Outline each blood parasite and name the species.
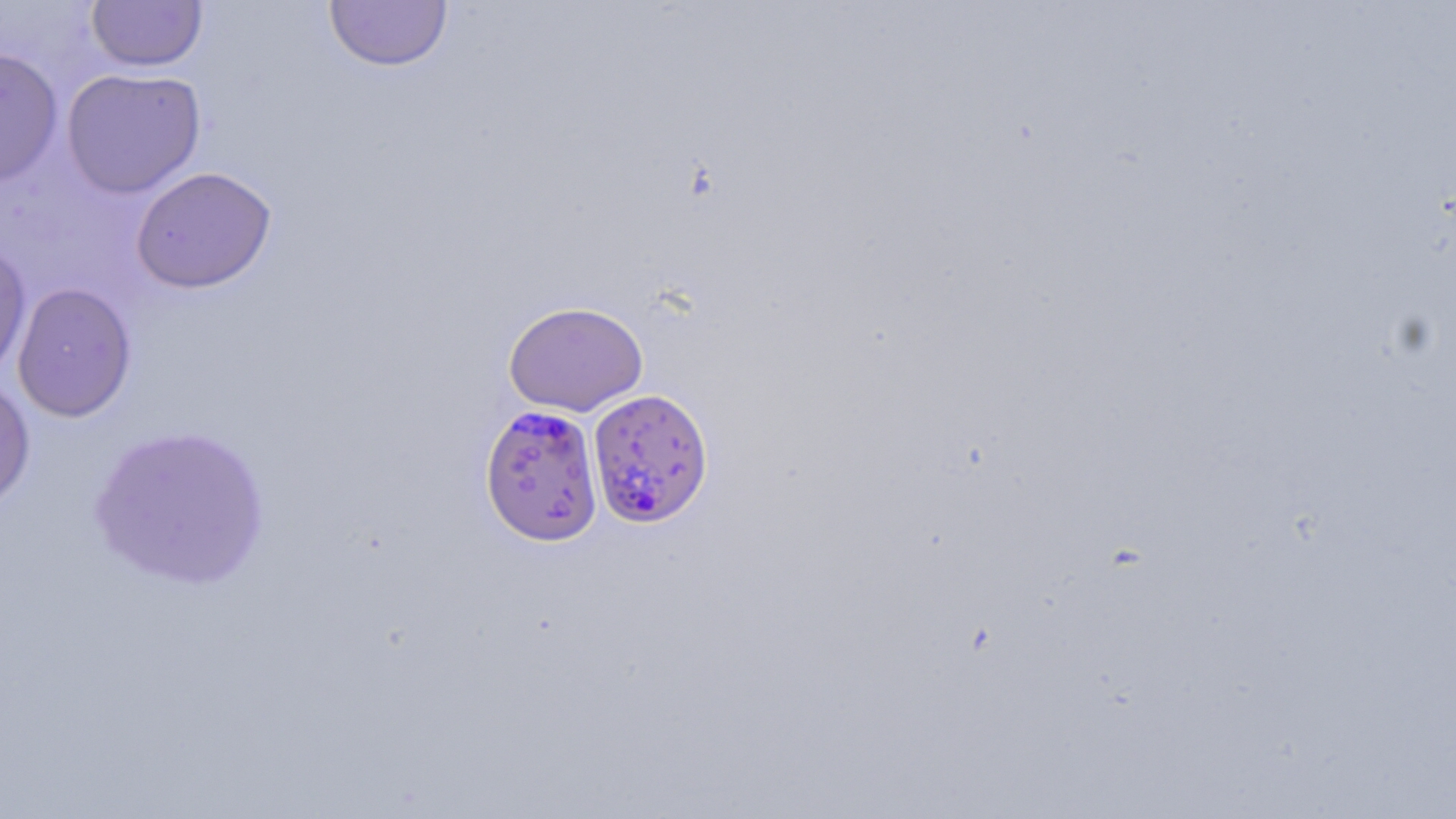

Approximate bounding boxes as (x1, y1, x2, y2) in pixels.
Plasmodium falciparum-infected red blood cells: (587, 388, 714, 528), (479, 404, 604, 546).
No Plasmodium ovale, Plasmodium malariae, Plasmodium vivax, Babesia divergens, or Trypanosoma brucei observed.

Uninfected red blood cell locations: (86, 0, 208, 72), (324, 1, 453, 72), (0, 46, 64, 188), (61, 67, 207, 199), (130, 166, 277, 294), (0, 240, 32, 382), (12, 282, 137, 423), (503, 300, 649, 416), (0, 373, 36, 515), (88, 423, 272, 591). Slide-level diagnosis: Plasmodium falciparum. Image is 1456×819 pixels. Optical microscopy. One field of a larger specimen. 1000x magnification. Thin blood film. May-Grünwald-Giemsa-stained preparation.